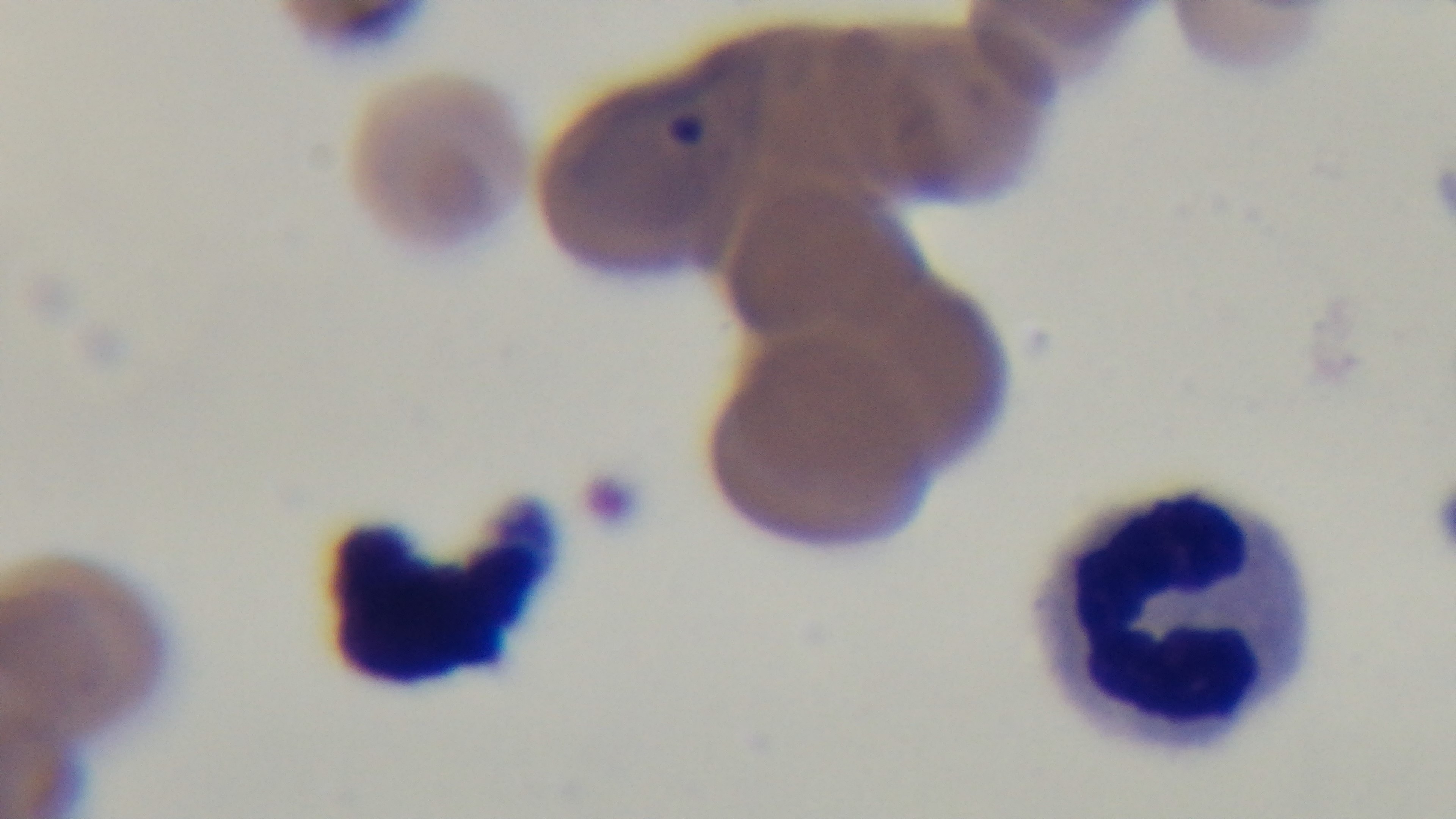

preparation: thin smear
modality: light microscopy
stain: Giemsa
objective: 100x oil immersion
field_of_view: one from the slide
malaria_status: infected
capture: mounted 4K digital camera